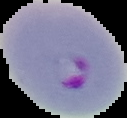
Summary:
  - Preparation: thin blood film
  - Image type: cell region segmented out of the field of view; surrounding area masked to black
  - Malaria status: parasitized
  - Image size: 127×118 pixels